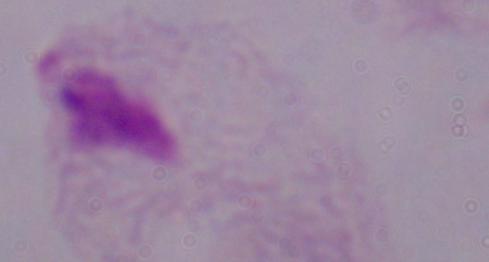
1000x magnification. A trichomonad is shown. Micrograph.